Assess the morphology of the erythrocytes.
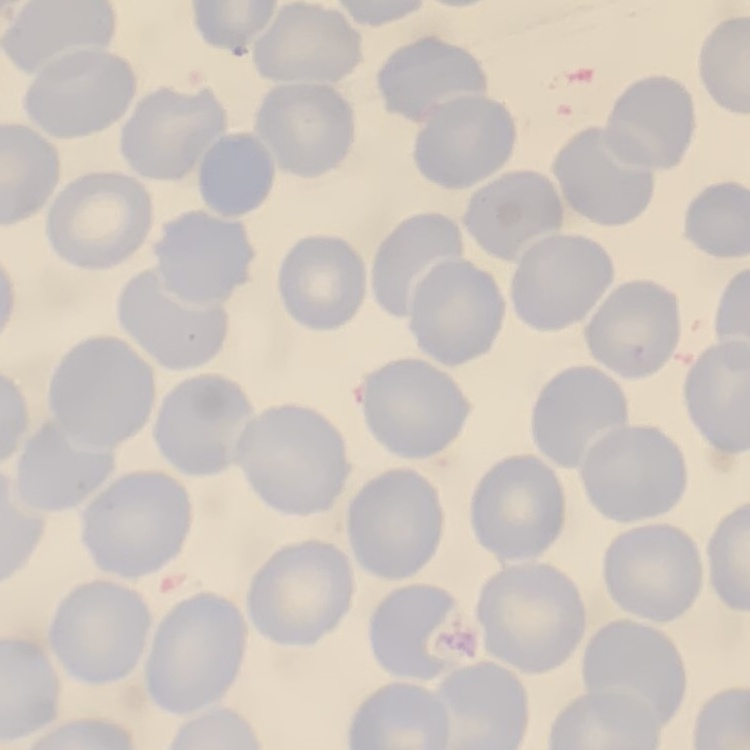
They show no rouleaux formation.

{
  "stain": "Field's or Giemsa",
  "image_type": "square crop of a larger photomicrograph",
  "preparation": "thin blood film"
}